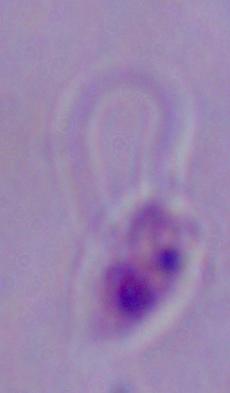
{
  "identification": "Leishmania",
  "magnification": "1000x",
  "modality": "photomicrograph"
}